Name the blood parasite species.
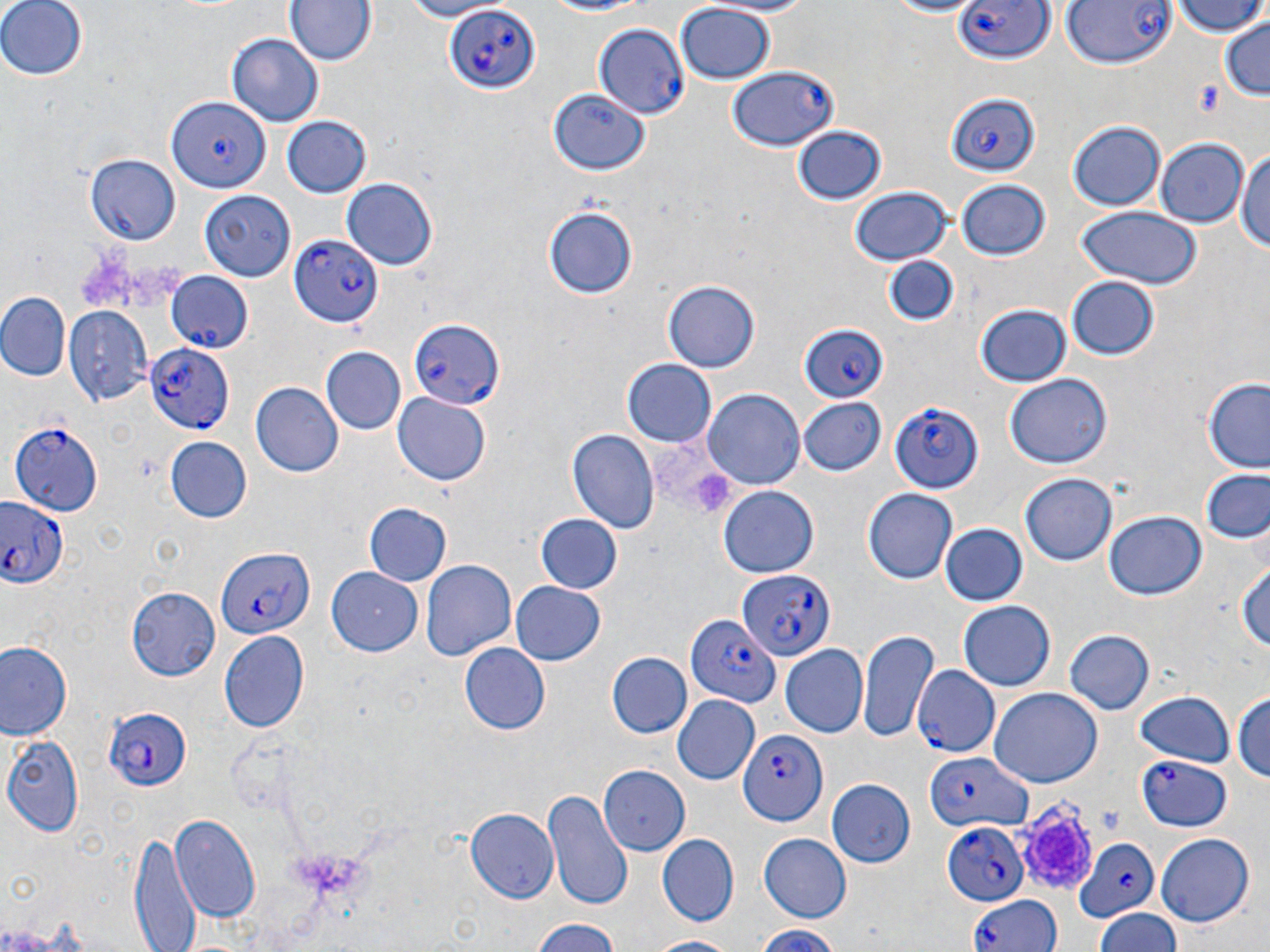
Plasmodium falciparum.

{
  "image_size": "1270×952 pixels",
  "platelet_locations": "approximate bounding boxes as (x1, y1, x2, y2) in pixels: (1195, 81, 1226, 119), (1021, 798, 1096, 886)",
  "stain": "May-Grünwald-Giemsa",
  "field_of_view": "single",
  "plasmodium_falciparum_infected_red_blood_cell_locations_subset": "approximate bounding boxes as (x1, y1, x2, y2) in pixels: (956, 0, 1054, 67), (444, 5, 541, 96), (593, 23, 688, 118), (730, 68, 838, 151), (944, 93, 1040, 176), (166, 97, 271, 192), (290, 235, 384, 327), (407, 317, 502, 409), (798, 325, 893, 404), (145, 344, 235, 432), (886, 398, 983, 492), (12, 421, 103, 513), (0, 495, 70, 591), (214, 547, 312, 639), (737, 571, 834, 662), (685, 612, 781, 708), (914, 665, 999, 755), (101, 705, 193, 793), (739, 729, 830, 824), (923, 753, 1029, 833), (1137, 755, 1232, 832), (940, 820, 1029, 907), (1072, 838, 1161, 921), (965, 891, 1061, 952)",
  "uninfected_red_blood_cell_locations_subset": "approximate bounding boxes as (x1, y1, x2, y2) in pixels: (0, 0, 85, 81), (390, 0, 507, 22), (533, 0, 660, 19), (697, 0, 819, 16), (877, 0, 984, 17), (1171, 0, 1265, 38), (287, 1, 375, 66), (674, 2, 774, 86), (1193, 4, 1270, 70), (1221, 18, 1270, 101), (228, 32, 324, 126), (549, 87, 649, 175), (280, 116, 372, 199), (1069, 121, 1165, 211), (791, 125, 888, 207), (1155, 138, 1245, 225), (1236, 142, 1270, 260), (84, 154, 181, 244), (342, 178, 439, 270), (956, 179, 1053, 262), (849, 187, 952, 264), (199, 188, 293, 280), (543, 205, 641, 299), (1074, 206, 1202, 287), (883, 255, 959, 328), (1064, 275, 1161, 362), (663, 278, 758, 375), (0, 290, 70, 382), (974, 302, 1073, 387), (65, 307, 152, 407), (320, 347, 405, 435), (621, 360, 717, 449), (1004, 374, 1109, 471), (1201, 377, 1270, 473), (250, 381, 341, 476), (703, 388, 804, 492), (392, 393, 492, 486), (797, 397, 886, 475), (566, 428, 659, 537), (165, 438, 251, 523), (1196, 470, 1270, 545), (1020, 473, 1117, 567), (718, 485, 819, 580), (862, 488, 957, 585), (364, 504, 451, 586), (533, 512, 624, 596), (1105, 512, 1206, 600), (938, 522, 1028, 606), (1235, 559, 1270, 661), (420, 560, 516, 664), (326, 568, 423, 655), (512, 579, 606, 667), (127, 587, 219, 681), (958, 601, 1055, 691), (859, 629, 938, 743), (1063, 629, 1154, 717), (218, 630, 309, 733), (0, 640, 74, 742), (459, 642, 550, 735), (779, 645, 870, 738), (607, 653, 692, 739), (989, 687, 1103, 787), (1132, 690, 1235, 768), (1232, 690, 1269, 787), (674, 695, 760, 785), (3, 733, 82, 836), (599, 765, 688, 854), (828, 779, 916, 867), (543, 789, 630, 908), (465, 809, 557, 904), (170, 816, 262, 924), (131, 830, 199, 952), (1154, 832, 1255, 928), (758, 833, 850, 922), (656, 834, 736, 927), (1094, 910, 1182, 952), (528, 919, 628, 952), (749, 922, 847, 952), (644, 935, 746, 952)",
  "modality": "light microscopy",
  "preparation": "thin blood smear",
  "magnification": "1000x"
}